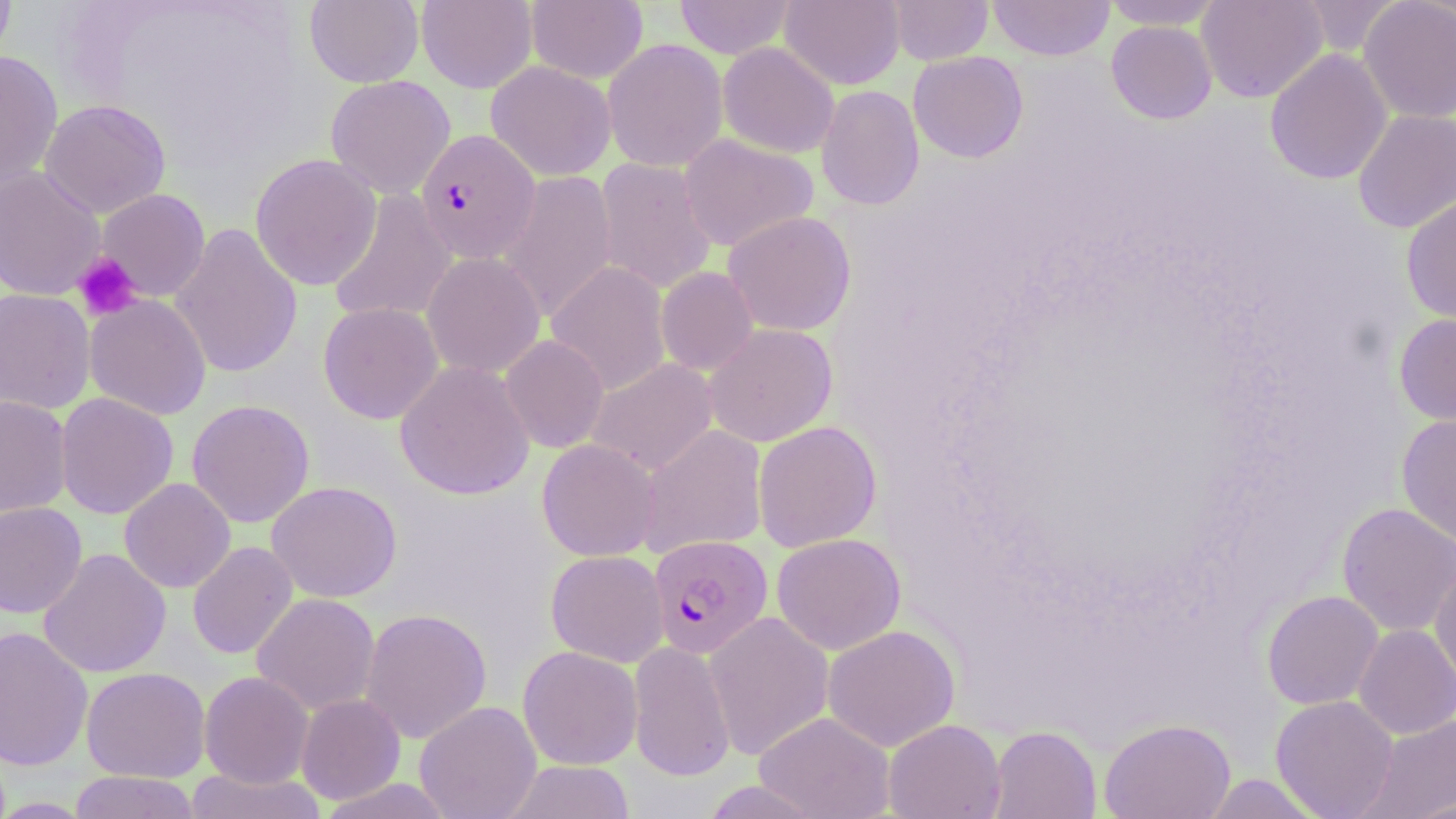
Summary:
  - Coordinate format: approximate bounding boxes as (x1, y1, x2, y2) in pixels
  - Plasmodium falciparum-infected red blood cell locations: (415, 129, 541, 264), (648, 535, 773, 658)
  - Platelet locations: (73, 252, 142, 321)
  - Uninfected red blood cell locations: (0, 0, 17, 69), (305, 0, 423, 88), (416, 0, 537, 93), (526, 0, 648, 83), (674, 0, 796, 59), (780, 0, 905, 90), (888, 0, 993, 65), (988, 0, 1115, 61), (1103, 0, 1225, 29), (1195, 0, 1327, 103), (1296, 0, 1403, 57), (1358, 0, 1456, 122), (1106, 21, 1217, 124), (603, 38, 728, 172), (717, 42, 840, 159), (0, 49, 63, 193), (1264, 49, 1392, 185), (908, 51, 1028, 163), (486, 60, 616, 181), (325, 75, 455, 198), (816, 85, 924, 210), (39, 99, 171, 218), (1352, 108, 1456, 233), (678, 134, 819, 252), (250, 153, 382, 291), (594, 158, 718, 295), (0, 166, 106, 301), (497, 170, 618, 323), (95, 188, 210, 302), (327, 189, 457, 326), (1401, 192, 1456, 326), (722, 211, 857, 336), (170, 222, 303, 379), (422, 252, 545, 378), (546, 261, 671, 395), (656, 267, 758, 375), (0, 288, 96, 415), (84, 294, 212, 420), (318, 302, 443, 424), (1394, 313, 1456, 426), (704, 323, 837, 447), (500, 334, 609, 453), (585, 358, 718, 475), (395, 360, 535, 501), (55, 392, 179, 519), (0, 395, 72, 519), (186, 399, 315, 528), (1396, 412, 1456, 547), (753, 420, 882, 552), (639, 424, 768, 556), (537, 438, 661, 561), (119, 477, 236, 593), (266, 480, 402, 603), (0, 501, 87, 618), (1336, 502, 1456, 637), (772, 533, 906, 655), (187, 541, 298, 660), (38, 548, 171, 678), (545, 550, 669, 667), (1429, 559, 1456, 688), (1261, 590, 1383, 710), (252, 593, 380, 716), (360, 607, 492, 744), (704, 611, 834, 761), (1354, 624, 1456, 739), (0, 625, 93, 771), (822, 625, 960, 752), (628, 640, 735, 781), (518, 646, 642, 770), (81, 666, 210, 783), (198, 671, 314, 788), (296, 694, 405, 804), (1270, 695, 1399, 818), (415, 701, 542, 819), (755, 712, 895, 819), (1358, 714, 1456, 818), (1099, 717, 1235, 819), (883, 719, 1006, 819), (988, 725, 1102, 819), (503, 760, 635, 818), (185, 767, 325, 819), (69, 770, 200, 819), (1201, 773, 1325, 817), (318, 778, 456, 818), (699, 780, 826, 819), (1401, 794, 1456, 818), (0, 797, 94, 818)
  - Slide-level diagnosis: Plasmodium falciparum
  - Field of view: single
  - Magnification: 1000x
  - Modality: light microscopy
  - Preparation: thin blood smear
  - Stain: May-Grünwald-Giemsa
  - Image size: 1456×819 pixels